Point out each Plasmodium parasite.
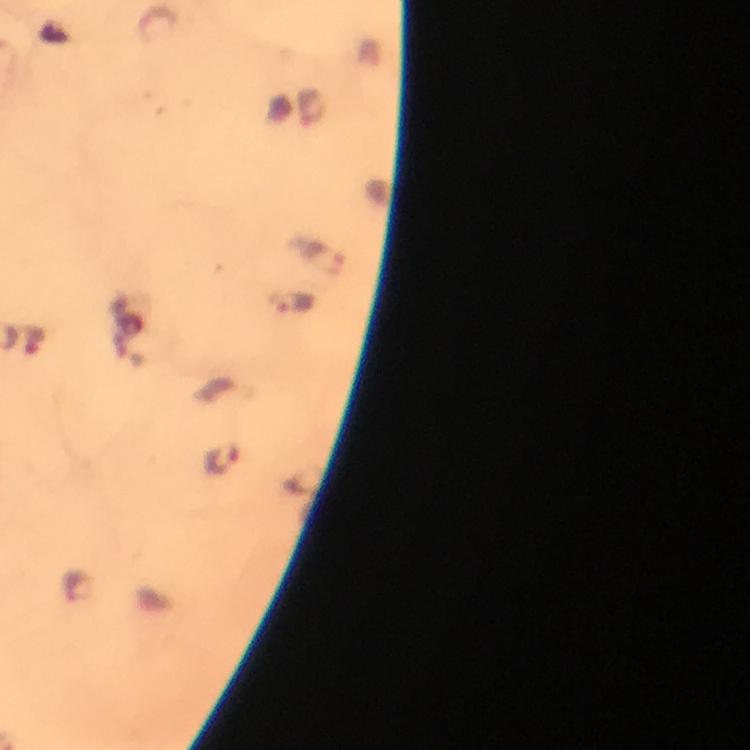

Approximate object centers, in pixels from the top-left corner.
Plasmodium parasites: (x=322, y=257), (x=293, y=304), (x=32, y=341), (x=222, y=461), (x=78, y=586).

Summary:
  - Image size: 750×750 pixels
  - Cropped from: a single field of view
  - Context: from a diagnostic examination for malaria
  - Stain: Giemsa
  - Capture: smartphone camera through the microscope
  - Preparation: thick blood film
  - Immersion oil: applied
  - Magnification: 100x